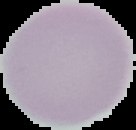
result = no malaria parasites detected
image size = 136×130 pixels
preparation = thin blood smear
image type = cell region segmented out of the field of view; surrounding area masked to black